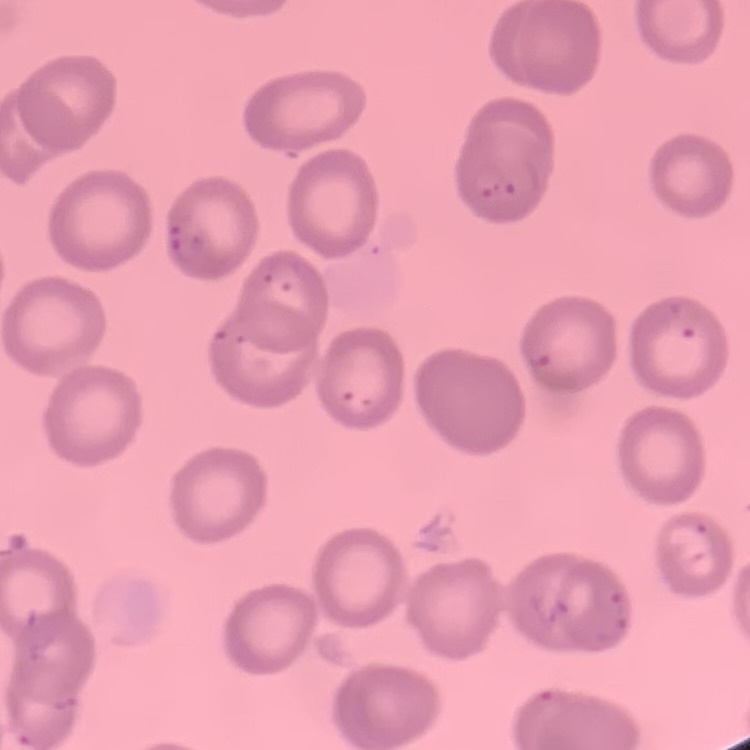

Summary:
  - Red blood cell morphology: no rouleaux formation
  - Image type: one tile cut from a larger photomicrograph
  - Preparation: thin blood film
  - Stain: Field's or Giemsa